Name the cell type shown.
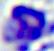
This is a leukocyte.

magnification = 400x
modality = photomicrograph